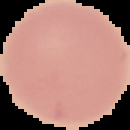

preparation = thin blood smear
image type = segmented cell region with the area outside set to black
result = no malaria parasites detected
image size = 130×130 pixels